Describe the morphology of the erythrocytes.
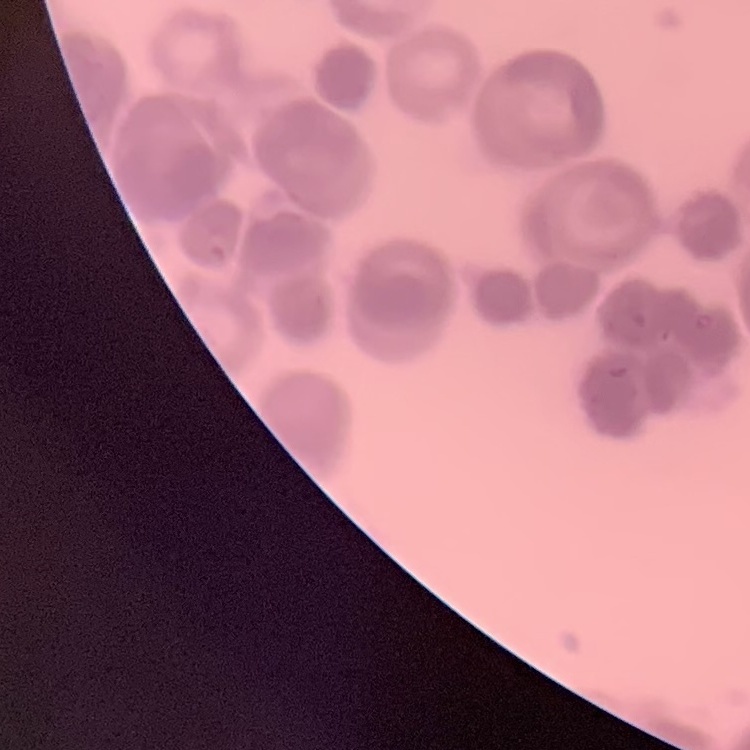

Rouleaux formation.

Square crop of a larger photomicrograph. Field's or Giemsa stain. Thin peripheral smear.